Report the malaria status of this cell.
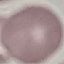

It is uninfected.

Summary:
  - Stain: Giemsa
  - Image type: cell patch, automatically extracted from a larger field of view and resized to 64 × 64 pixels
  - Capture: smartphone camera at the microscope eyepiece
  - Preparation: thin smear